Identify the cell.
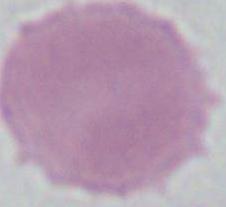

An erythrocyte.

modality = photomicrograph
magnification = 1000x